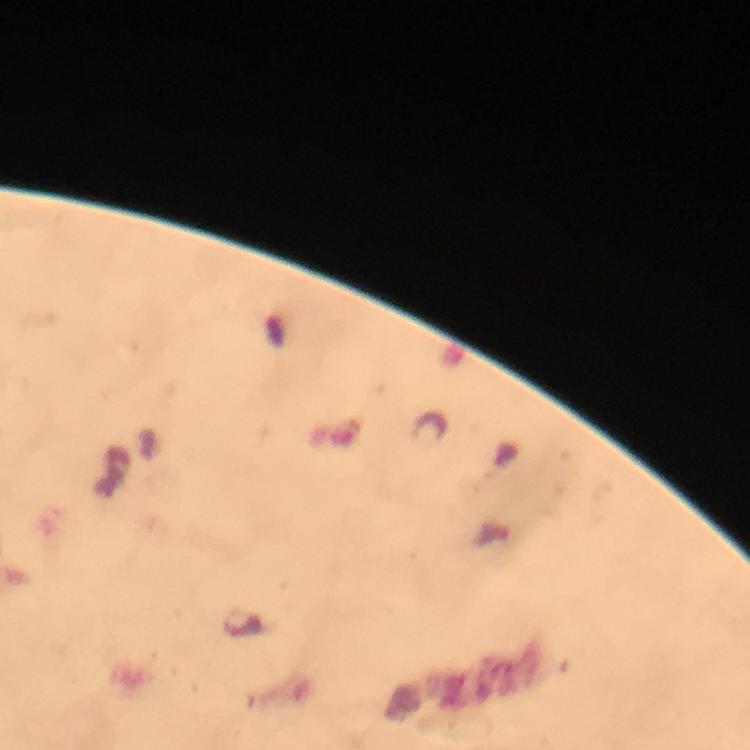

preparation: thick smear
image_size: 750×750 pixels
context: from a malaria diagnostic workup
immersion_oil: used
stain: Giemsa
magnification: 100x
plasmodium_parasite_locations: 'approximate centers as (x, y) in pixels: (242, 624)'
capture: smartphone camera through the microscope
cropped_from: one field of view